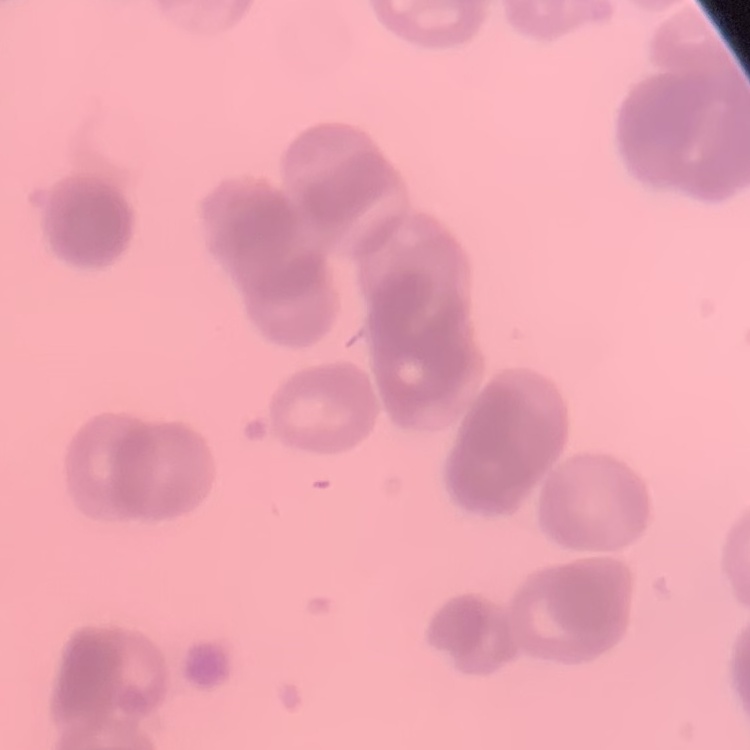
red blood cell morphology = rouleaux formation
image type = square crop of a larger photomicrograph
preparation = thin blood film
stain = Field's or Giemsa